Report the malaria status of this cell.
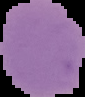

It is uninfected.

preparation: thin blood smear
image_size: 85×97 pixels
image_type: cell region segmented out of the field of view; surrounding area masked to black